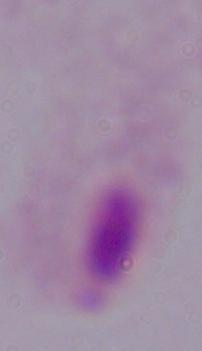 1000x magnification. A trichomonad is shown. Photomicrograph.